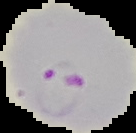
Malaria status: parasitized. The area outside the segmented cell region is set to black. Image is 136×133 pixels. From a thin blood smear.